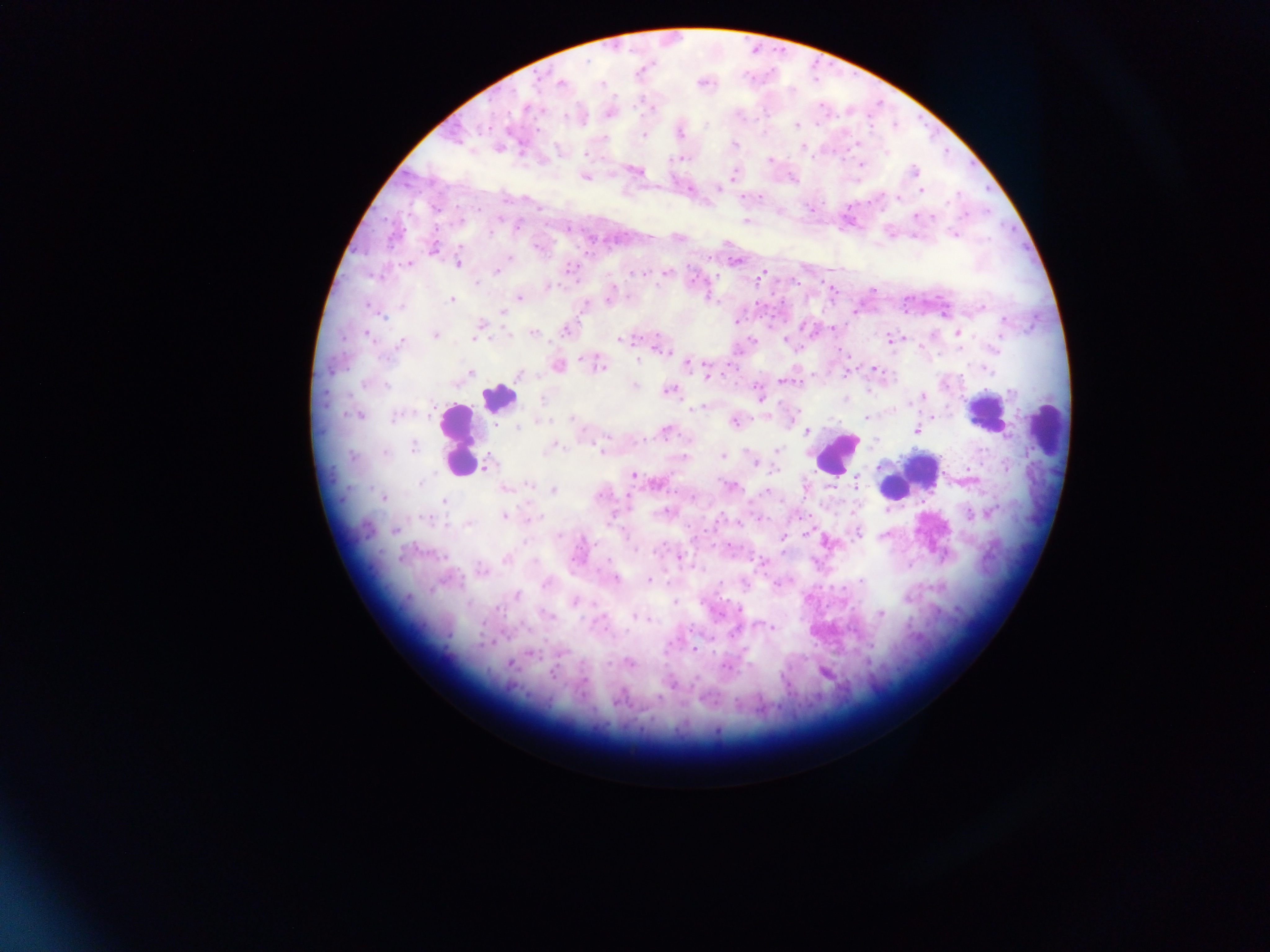
{
  "image_size": "1270×952 pixels",
  "malaria_parasite_locations": "approximate centers as x y in pixels: 538 81; 561 82; 601 85; 610 113; 706 124; 796 125; 488 126; 680 133; 644 135; 603 139; 734 143; 802 146; 886 152; 586 155; 675 158; 770 159; 861 164; 914 170; 638 171; 734 174; 583 176; 718 188; 921 190; 760 197; 898 198; 435 208; 915 216; 746 221; 518 225; 490 232; 953 234; 677 238; 433 248; 510 258; 735 262; 409 263; 457 264; 569 268; 497 271; 667 272; 633 274; 639 274; 762 274; 477 283; 549 286; 831 289; 520 298; 609 299; 452 300; 585 305; 370 307; 402 307; 982 308; 502 310; 382 317; 737 321; 1005 321; 480 327; 833 327; 566 330; 958 332; 534 334; 435 335; 509 335; 657 335; 368 336; 474 338; 890 338; 998 339; 620 340; 751 340; 785 340; 401 342; 995 348; 663 350; 583 359; 637 361; 686 364; 558 366; 599 366; 875 368; 988 371; 847 372; 471 373; 519 375; 709 376; 784 381; 366 384; 634 385; 386 386; 758 390; 668 391; 869 391; 1010 392; 759 396; 923 397; 542 399; 910 402; 698 408; 798 411; 356 415; 395 417; 763 417; 866 417; 932 417; 571 418; 543 422; 734 422; 517 428; 916 430; 807 431; 665 432; 607 438; 413 447; 551 448; 777 450; 601 451; 386 452; 723 456; 352 457; 755 463; 488 464; 1006 467; 775 471; 633 476; 420 483; 655 483; 855 484; 530 485; 729 485; 505 488; 553 490; 766 491; 383 498; 443 500; 664 511; 990 512; 505 516; 970 516; 538 517; 426 518; 759 519; 610 520; 468 524; 395 530; 806 531; 857 533; 560 536; 783 538; 661 548; 635 550; 679 557; 506 559; 762 563; 481 571; 616 578; 649 580; 860 580; 720 583; 545 585; 516 596; 575 602; 674 602; 468 604; 739 609; 880 613; 548 615; 633 617; 649 619; 603 624; 772 627; 733 632; 694 649; 530 653; 562 653; 510 663; 630 663; 607 664; 726 667; 553 673; 696 677; 584 681; 672 684; 717 731",
  "field_of_view": "single",
  "leukocyte_locations": "approximate centers as x y in pixels: 498 397; 984 412; 1046 431; 457 440; 836 453; 921 468; 892 487",
  "preparation": "thick blood film",
  "country": "Ghana",
  "capture": "mobile-phone photograph through a microscope"
}